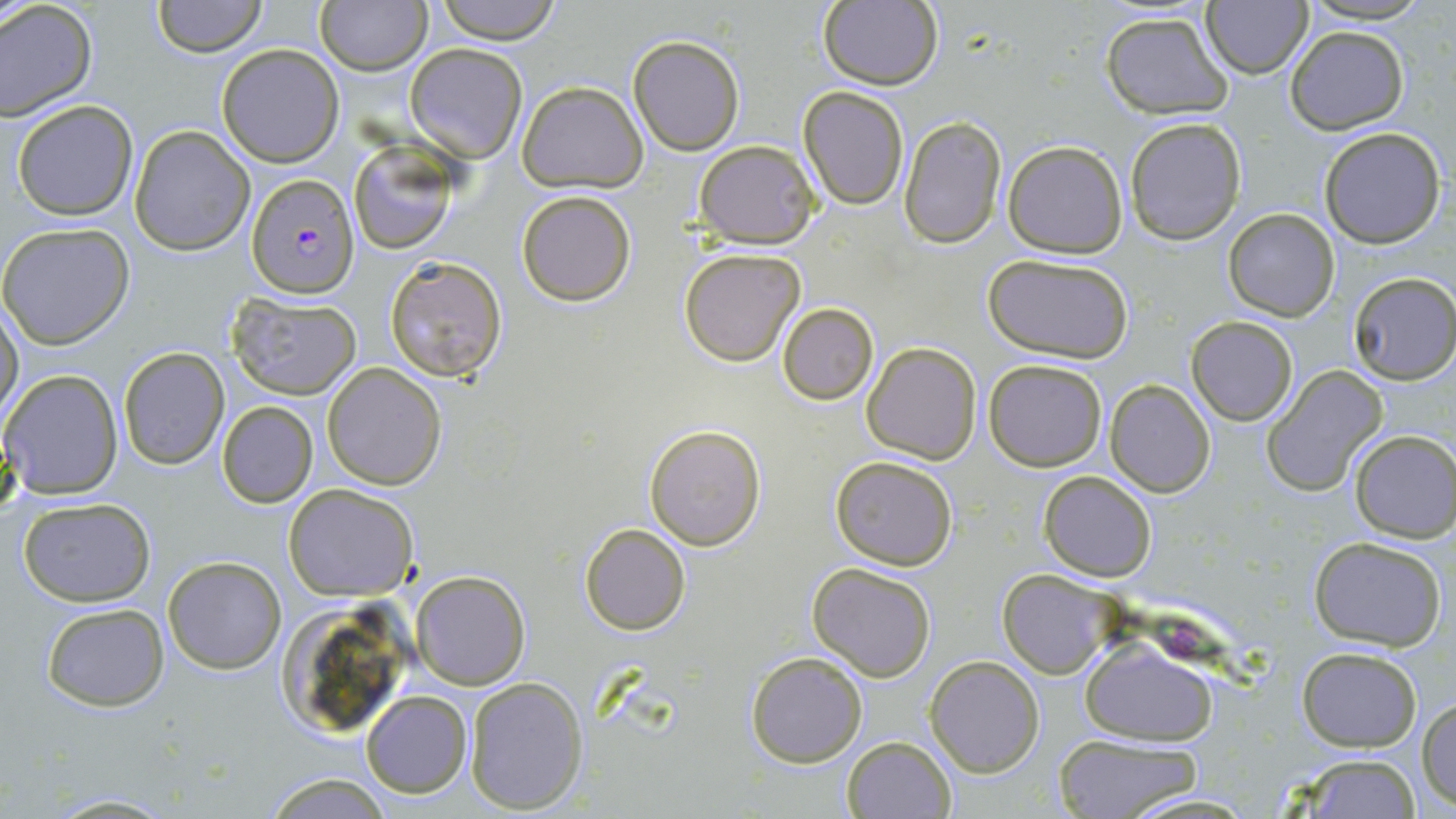

Summary:
  - Coordinate format: approximate bounding boxes as (x1,y1)-(x2,y2) corner pairs in pixels
  - Plasmodium falciparum-infected red blood cell locations: (246,175)-(360,299)
  - Uninfected red blood cell locations: (152,0)-(267,57), (432,0)-(562,43), (1299,0)-(1433,25), (316,1)-(430,75), (817,1)-(943,90), (0,2)-(98,123), (1201,3)-(1314,79), (1101,10)-(1232,120), (1286,26)-(1408,134), (626,33)-(744,156), (405,43)-(529,162), (216,44)-(345,166), (517,81)-(647,194), (798,87)-(910,210), (11,100)-(139,221), (897,116)-(1008,249), (1125,117)-(1247,245), (128,125)-(255,255), (1318,127)-(1446,247), (694,139)-(821,249), (1001,139)-(1128,258), (348,145)-(457,256), (516,190)-(636,306), (1224,208)-(1340,321), (0,222)-(134,349), (679,247)-(806,366), (983,253)-(1136,365), (384,256)-(508,384), (1349,273)-(1456,384), (226,292)-(363,400), (776,302)-(879,406), (1,304)-(25,422), (1186,316)-(1298,425), (861,343)-(981,464), (118,347)-(229,470), (983,358)-(1107,472), (322,363)-(447,491), (1,368)-(123,500), (1263,368)-(1389,496), (1104,380)-(1216,497), (216,400)-(318,509), (643,423)-(766,551), (1350,430)-(1456,542), (830,455)-(961,570), (1038,470)-(1158,583), (284,483)-(419,600), (16,496)-(156,607), (580,523)-(690,636), (1307,535)-(1449,649), (164,556)-(286,674), (807,563)-(937,682), (411,569)-(531,691), (998,570)-(1125,678), (273,600)-(409,738), (40,602)-(168,712), (1079,639)-(1220,744), (1297,646)-(1422,751), (745,651)-(867,768), (925,655)-(1046,777), (463,677)-(589,814), (361,691)-(471,798), (1419,696)-(1455,809), (1054,734)-(1201,817), (841,735)-(956,818), (1287,752)-(1424,818), (263,770)-(393,818), (42,792)-(181,817), (1118,792)-(1262,817)
  - Slide-level diagnosis: Plasmodium falciparum
  - Field of view: one of a larger specimen
  - Magnification: 1000x
  - Modality: optical microscopy
  - Stain: May-Grünwald-Giemsa
  - Image size: 1456×819 pixels
  - Preparation: thin blood smear